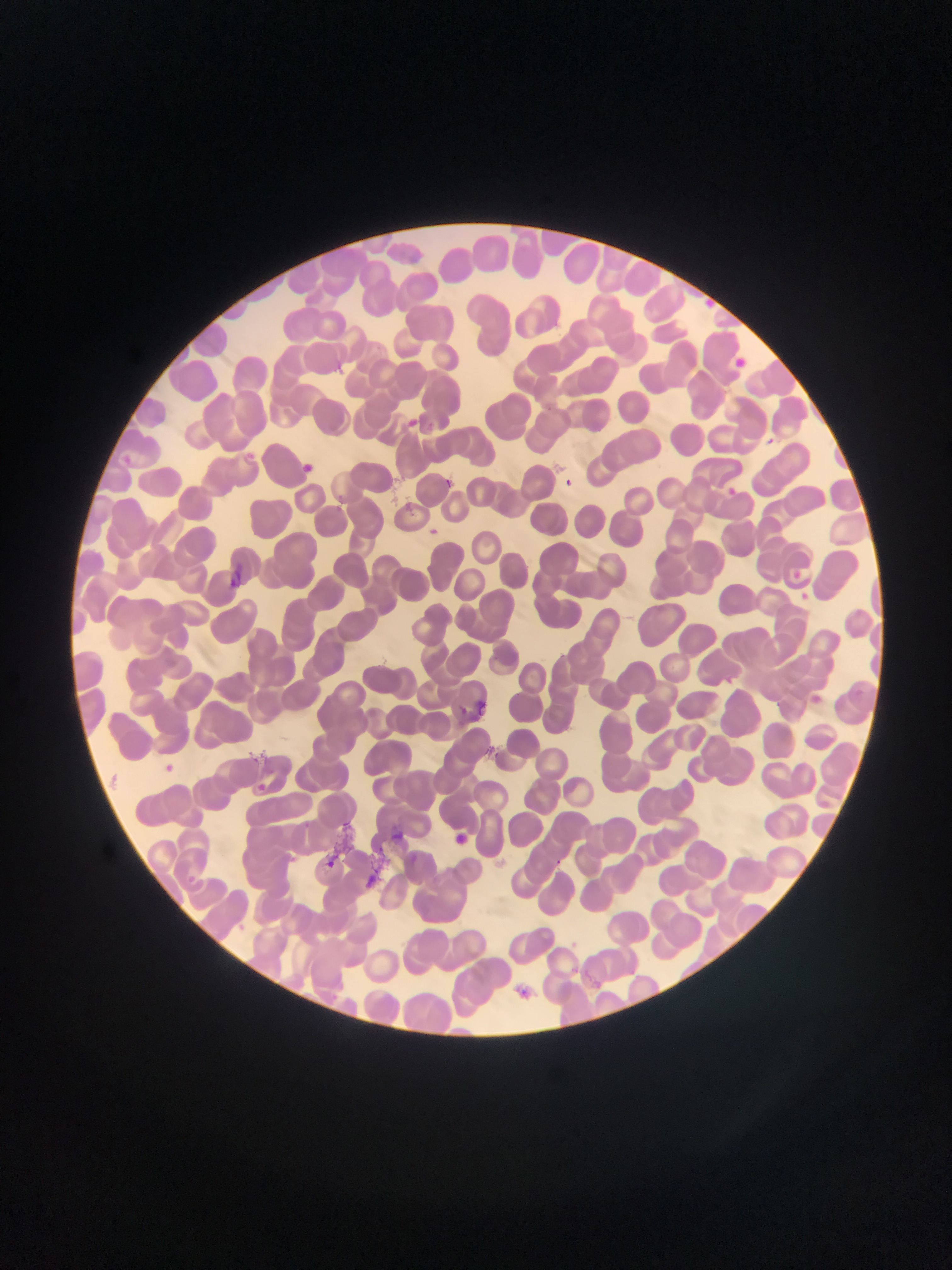
country: Ghana
capture: mobile-phone photograph through a microscope
malaria_parasite_locations: 'approximate bounding boxes as [left, top, right, bottom] in pixels: [699, 295, 718, 314], [738, 355, 751, 372], [407, 415, 419, 425], [763, 429, 778, 446], [296, 459, 326, 480], [440, 473, 465, 495], [560, 473, 580, 495], [729, 481, 738, 493], [428, 522, 442, 538], [227, 562, 242, 599], [788, 564, 807, 576], [472, 699, 499, 716], [159, 758, 185, 782], [253, 775, 274, 797], [389, 827, 404, 845], [455, 834, 472, 847], [326, 848, 351, 879], [369, 861, 382, 888], [510, 985, 525, 1002]'
field_of_view: single
image_size: 952×1270 pixels
preparation: thin blood film